Name the parasite shown.
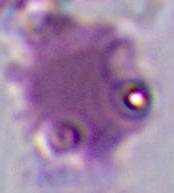

This is Plasmodium.

Summary:
  - Magnification: 400x or 1000x
  - Modality: photomicrograph